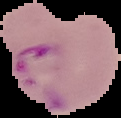

Malaria status: parasitized. Segmented cell region on a black background. From a thin blood smear. Image is 121×118 pixels.